Assess this cell for malaria.
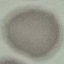

Uninfected.

Acquired by smartphone through the microscope eyepiece. Giemsa stain. Automatically extracted cell patch, resized to 64 × 64 pixels. Thin blood film.